Classify this cell by malaria status.
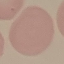
It is uninfected.

Giemsa stain. Cell patch, automatically extracted from a larger field of view and resized to 64 × 64 pixels. Thin smear of blood. Photographed with a smartphone camera at the microscope eyepiece.